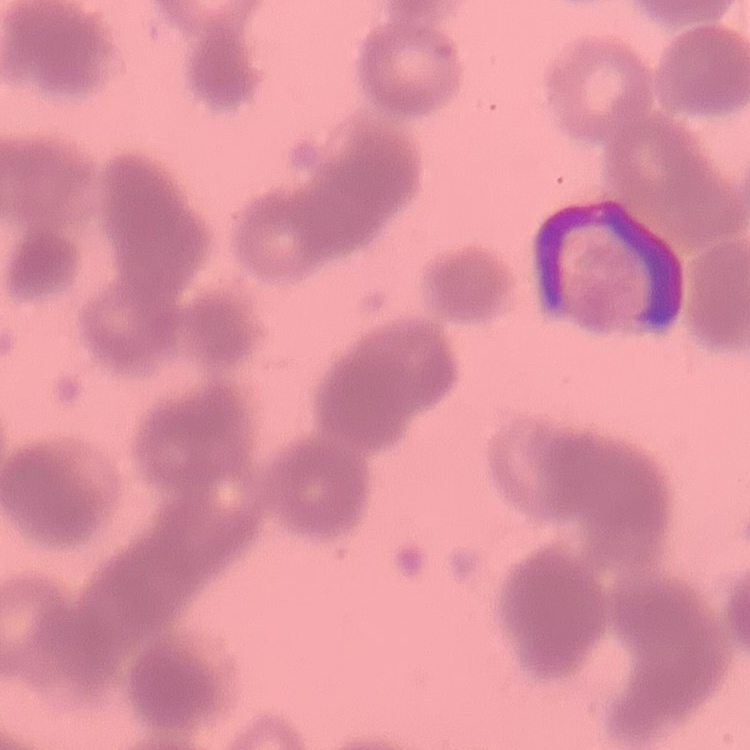 The red blood cells exhibit rouleaux formation. Thin blood smear. One tile cut from a larger photomicrograph. Stained with either Field's or Giemsa.